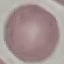
{
  "result": "no malaria parasites detected",
  "stain": "Giemsa",
  "image_type": "cell patch, automatically extracted from a larger field of view and resized to 64 × 64 pixels",
  "preparation": "thin blood smear",
  "capture": "smartphone camera at the microscope eyepiece"
}